Locate every Plasmodium malariae-infected red blood cell.
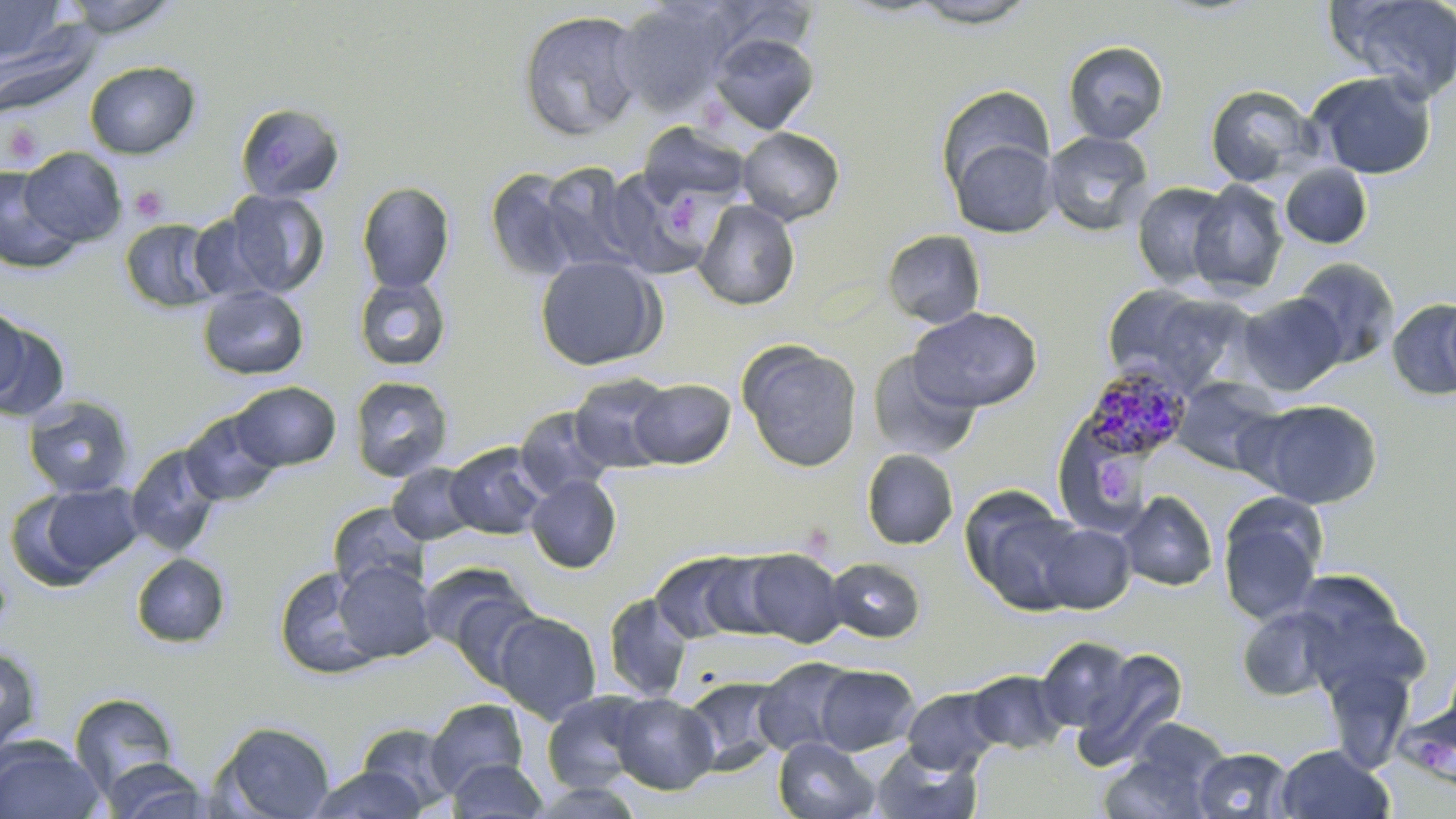

Approximate bounding boxes as (x1, y1, x2, y2) in pixels.
Plasmodium malariae-infected red blood cells: (1078, 365, 1192, 467).

Uninfected red blood cell locations: (0, 0, 63, 63), (62, 0, 181, 37), (905, 0, 1041, 29), (1327, 0, 1456, 103), (612, 1, 738, 115), (706, 1, 820, 58), (517, 10, 645, 142), (1, 22, 100, 119), (708, 32, 820, 134), (1062, 40, 1169, 144), (84, 61, 201, 159), (1307, 71, 1437, 180), (936, 84, 1056, 198), (1205, 84, 1321, 188), (235, 102, 346, 203), (637, 122, 753, 211), (736, 127, 845, 226), (1042, 130, 1155, 237), (947, 136, 1059, 238), (19, 147, 126, 247), (537, 163, 642, 273), (1279, 164, 1372, 250), (0, 165, 81, 274), (599, 168, 713, 278), (484, 169, 583, 282), (1187, 180, 1289, 297), (357, 181, 455, 293), (1132, 182, 1233, 289), (222, 190, 329, 297), (693, 200, 800, 311), (186, 214, 276, 302), (119, 217, 223, 314), (883, 229, 986, 328), (535, 255, 665, 371), (1291, 257, 1400, 368), (354, 276, 451, 371), (1101, 284, 1249, 396), (197, 286, 310, 380), (1237, 293, 1346, 395), (1387, 298, 1456, 401), (0, 306, 54, 415), (909, 306, 1042, 413), (738, 341, 863, 473), (867, 350, 980, 462), (568, 374, 676, 474), (349, 376, 454, 481), (1172, 376, 1283, 476), (629, 379, 735, 468), (230, 381, 341, 471), (22, 395, 136, 499), (1246, 398, 1383, 509), (514, 406, 616, 501), (180, 410, 284, 506), (1053, 416, 1157, 534), (444, 442, 550, 539), (125, 444, 225, 557), (861, 449, 959, 550), (387, 462, 480, 545), (525, 474, 622, 574), (17, 481, 145, 586), (961, 487, 1087, 615), (1118, 490, 1217, 592), (1217, 494, 1328, 626), (328, 502, 430, 596), (1033, 521, 1135, 613), (741, 548, 846, 647), (650, 550, 764, 644), (131, 553, 230, 648), (825, 557, 926, 643), (333, 561, 438, 663), (274, 565, 384, 681), (1286, 569, 1422, 693), (431, 572, 547, 687), (602, 592, 694, 702), (1236, 605, 1345, 702), (494, 611, 601, 724), (1035, 636, 1136, 732), (0, 643, 44, 755), (1074, 647, 1189, 768), (1317, 656, 1419, 774), (753, 657, 858, 756), (814, 664, 919, 755), (965, 669, 1070, 754), (681, 676, 789, 774), (902, 687, 1001, 774), (542, 690, 652, 793), (69, 692, 181, 797), (610, 693, 718, 794), (425, 699, 529, 795), (1128, 717, 1231, 794), (213, 721, 337, 818), (355, 721, 459, 812), (773, 736, 879, 819), (0, 737, 104, 818), (871, 741, 982, 819), (1275, 744, 1394, 819), (1193, 747, 1294, 819), (1100, 753, 1213, 819), (101, 757, 213, 818), (448, 758, 548, 818), (309, 765, 426, 819), (527, 781, 646, 818). Platelet locations: (3, 119, 45, 168), (129, 186, 168, 222), (665, 194, 708, 238), (0, 568, 14, 630). Slide-level diagnosis: Plasmodium malariae. May-Grünwald-Giemsa stain. Light microscopy. Single field of view. Image is 1456×819 pixels. Captured at 1000x magnification. Thin blood smear.